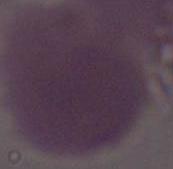

1000x magnification. A red blood cell is shown. Micrograph.